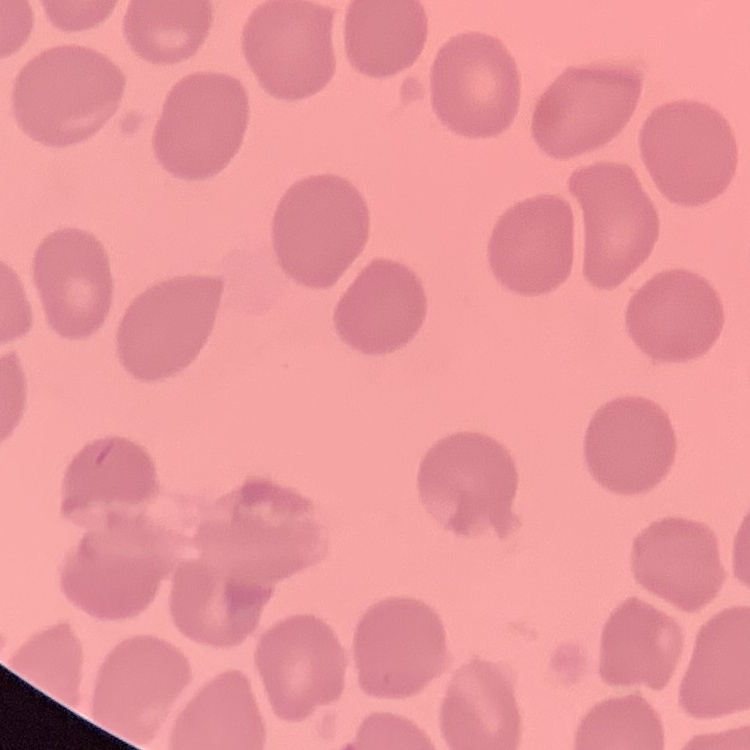

Summary:
  - Erythrocyte morphology: no rouleaux formation
  - Image type: one tile cut from a larger photomicrograph
  - Preparation: thin blood film
  - Stain: Field's or Giemsa